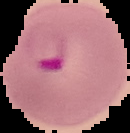
Image is 130×133 pixels. Malaria status: parasitized. Segmented cell region on a black background. From a thin blood smear.